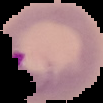

Summary:
  - Malaria status: parasitized
  - Image type: cell region segmented out of the field of view; surrounding area masked to black
  - Image size: 103×103 pixels
  - Preparation: thin blood film